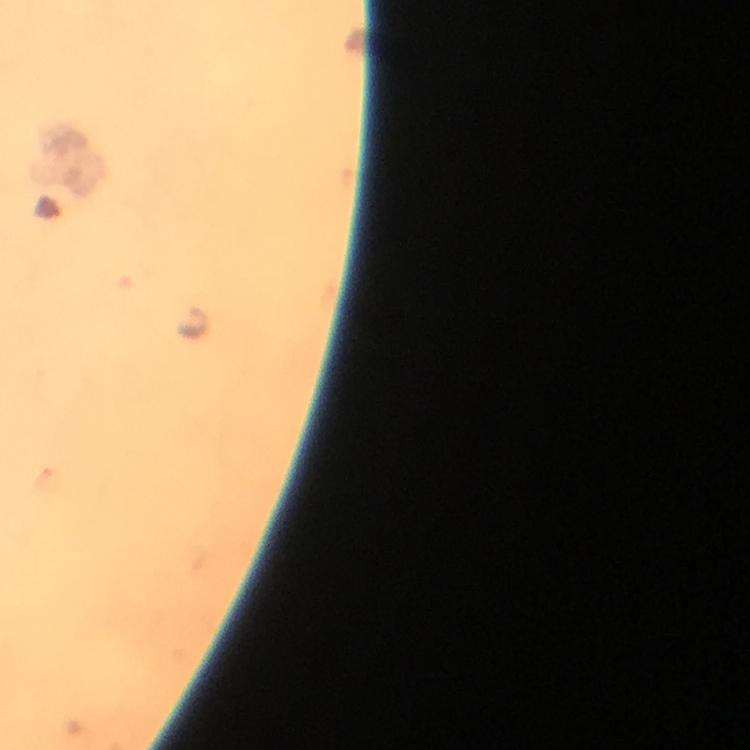 Approximate object centers, in pixels from the top-left corner. Malaria parasite locations: (x=193, y=324). Thick blood smear. Giemsa-stained preparation. Immersion oil was used. Image is 750×750 pixels. From a malaria diagnostic workup. Cropped region of a single field of view. 100x magnification. Photographed with a smartphone mounted on the microscope.